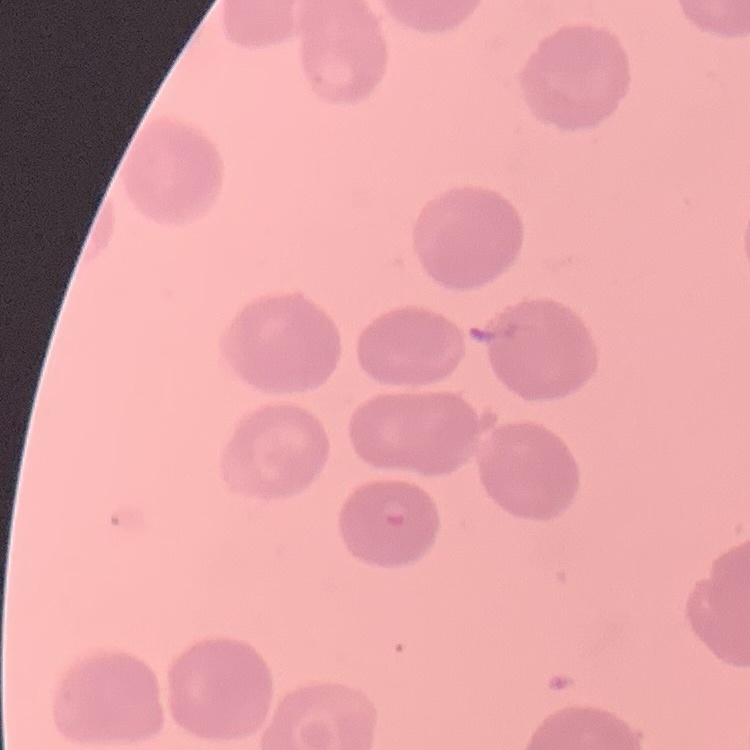

Summary:
  - Erythrocyte morphology: no rouleaux formation
  - Image type: one tile cut from a larger photomicrograph
  - Preparation: thin peripheral smear
  - Stain: Field's or Giemsa